Classify this cell by malaria status.
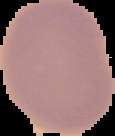

It is uninfected.

image type = cell region segmented out of the field of view; surrounding area masked to black
image size = 115×136 pixels
preparation = thin blood film